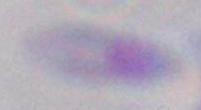

modality = photomicrograph
magnification = 1000x
identification = Toxoplasma gondii